Report the malaria status of this cell.
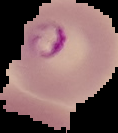

It is parasitized.

{
  "image_type": "cell region segmented out of the field of view; surrounding area masked to black",
  "image_size": "118×133 pixels",
  "preparation": "thin blood film"
}